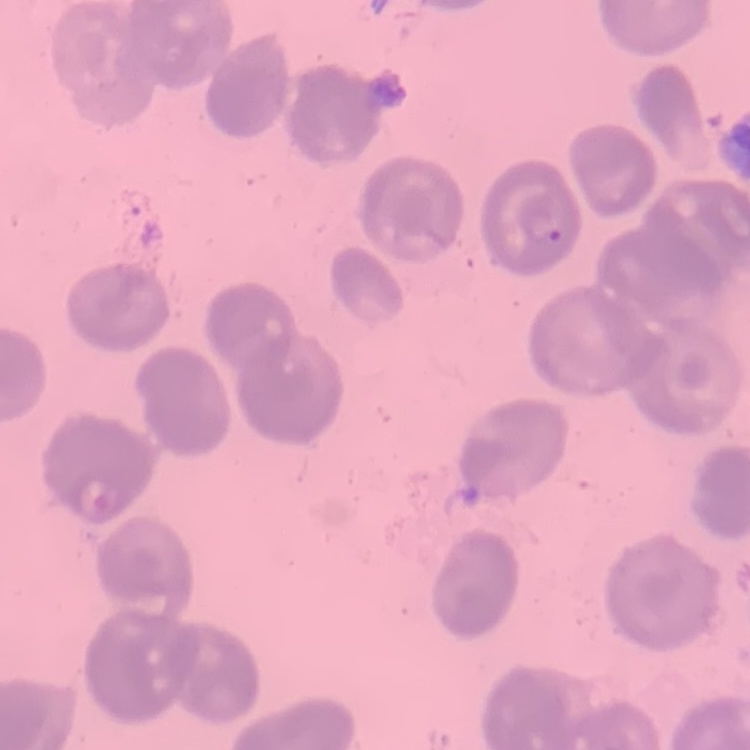

red blood cell morphology = no rouleaux formation
preparation = thin peripheral smear
stain = Field's or Giemsa
image type = one tile cut from a larger photomicrograph